Report the malaria status of this cell.
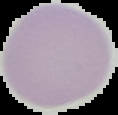
It is uninfected.

Cell region segmented out of the field of view; the surrounding area is masked to black. Image is 118×115 pixels. From a thin blood smear.